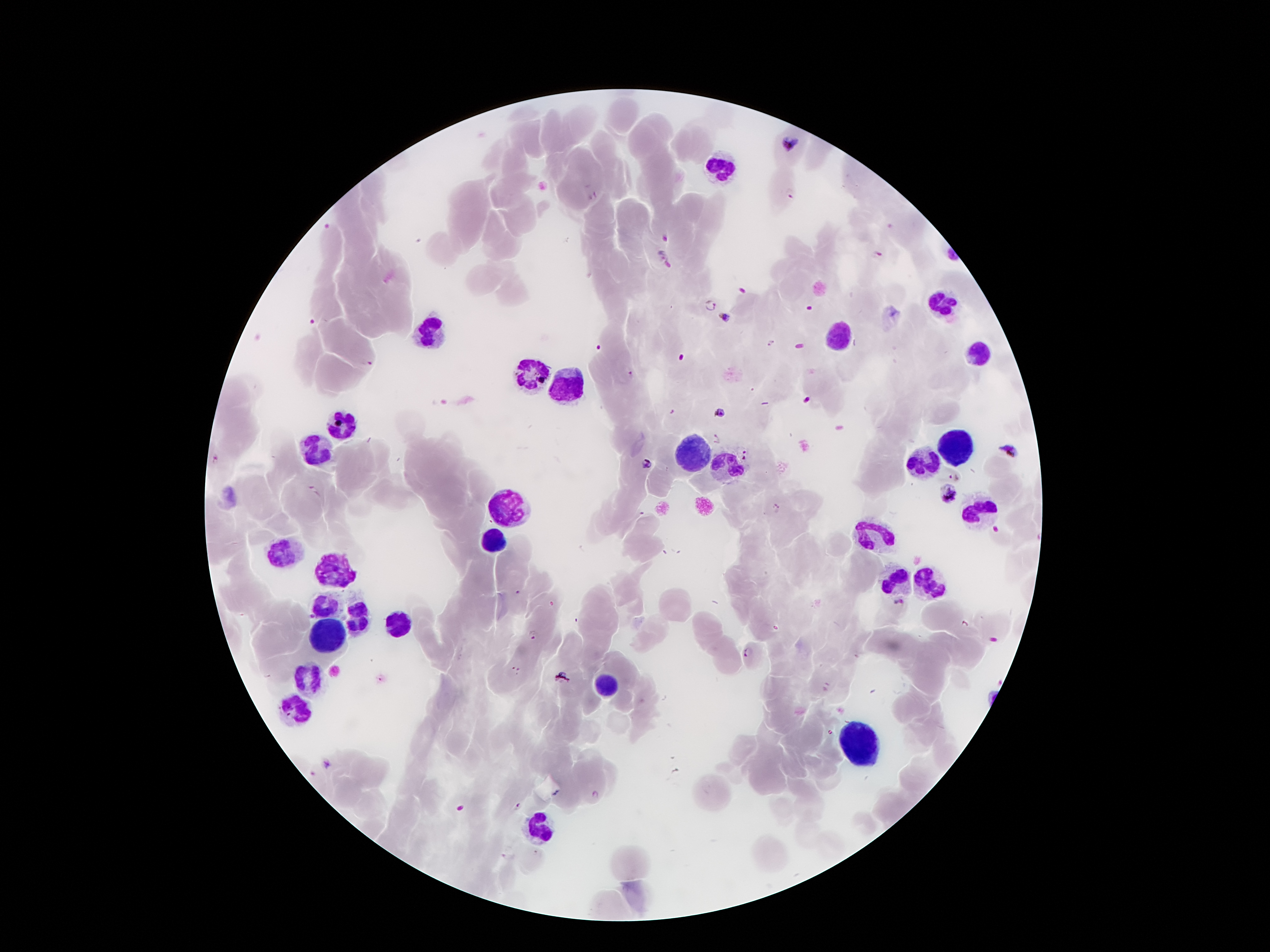
coordinate format = approximate object centers, in pixels from the top-left corner
leukocyte locations = (x=721, y=164), (x=940, y=300), (x=430, y=333), (x=841, y=333), (x=979, y=352), (x=529, y=371), (x=566, y=389), (x=346, y=425), (x=955, y=443), (x=316, y=447), (x=691, y=455), (x=729, y=462), (x=923, y=464), (x=507, y=507), (x=983, y=509), (x=493, y=537), (x=874, y=537), (x=281, y=554), (x=337, y=567), (x=897, y=582), (x=927, y=582), (x=325, y=604), (x=353, y=613), (x=394, y=623), (x=329, y=638), (x=310, y=677), (x=605, y=686), (x=292, y=705), (x=856, y=748), (x=540, y=832)
malaria parasite locations = (x=790, y=144), (x=790, y=193), (x=665, y=238), (x=876, y=254), (x=664, y=258), (x=708, y=305), (x=725, y=314), (x=771, y=342), (x=366, y=361), (x=630, y=375), (x=808, y=400), (x=720, y=412), (x=717, y=439), (x=745, y=450), (x=1008, y=452), (x=743, y=459), (x=646, y=463), (x=955, y=476), (x=948, y=496), (x=776, y=507), (x=900, y=604), (x=533, y=634), (x=748, y=652), (x=515, y=670), (x=561, y=676), (x=328, y=763), (x=595, y=794), (x=518, y=805)
field of view = one from this slide
capture = smartphone camera through the microscope eyepiece
preparation = thick peripheral-blood smear
image size = 1270×952 pixels
magnification = 100x
stain = Giemsa
patient malaria status = infected with Plasmodium falciparum